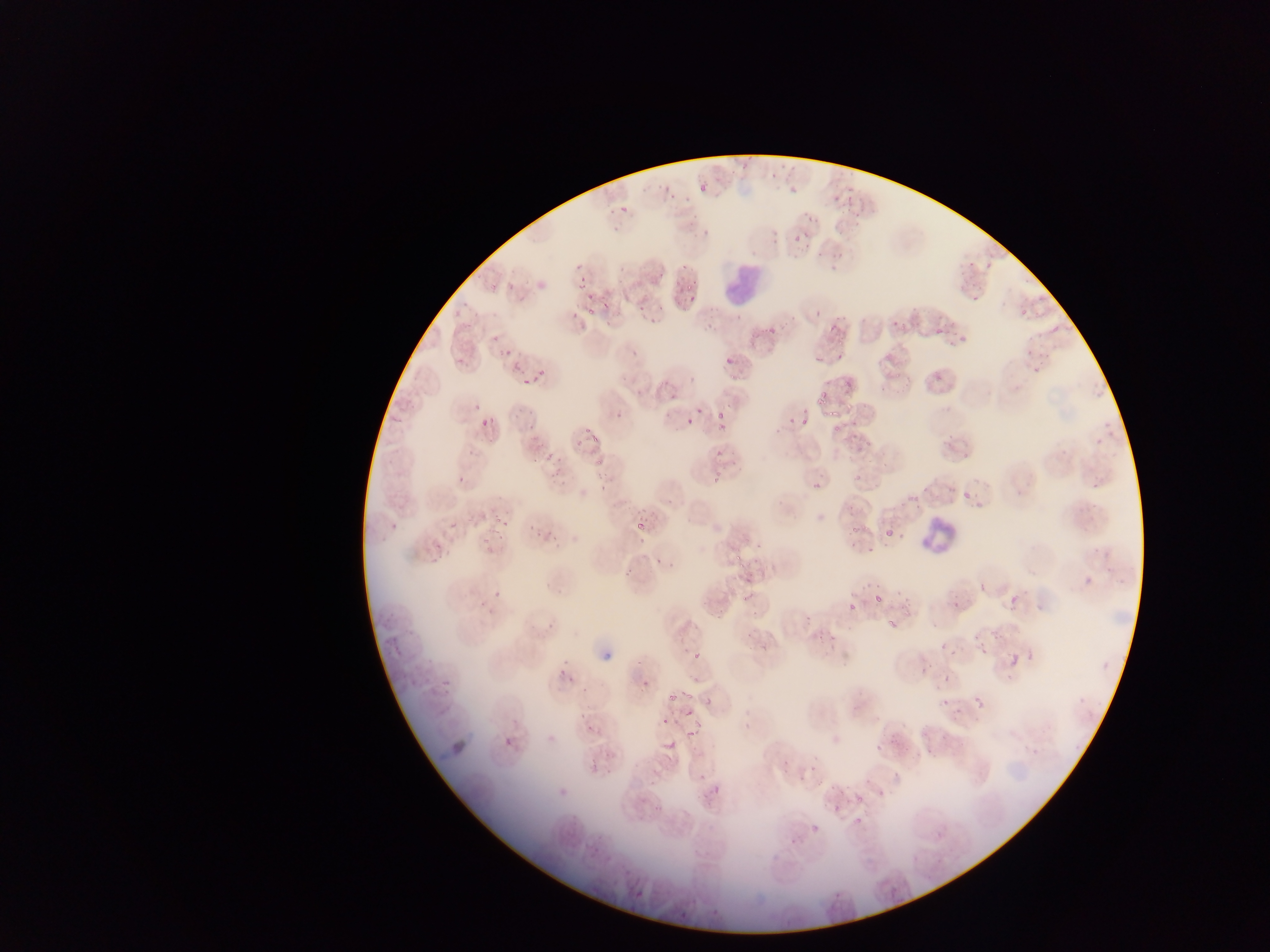

Approximate bounding boxes as [left, top, right, bottom] in pixels. Plasmodium parasite locations: [788, 223, 816, 250], [574, 274, 590, 296], [679, 286, 698, 304], [587, 303, 604, 321], [807, 310, 819, 319], [826, 321, 840, 339], [1050, 324, 1060, 333], [935, 327, 943, 334], [486, 334, 503, 346], [721, 343, 740, 366], [497, 347, 518, 365], [810, 354, 823, 366], [535, 368, 549, 385], [518, 380, 529, 388], [715, 399, 732, 430], [479, 415, 493, 428], [800, 415, 807, 425], [781, 417, 801, 426], [685, 418, 695, 427], [585, 434, 597, 447], [714, 447, 722, 458], [538, 458, 547, 467], [705, 470, 726, 490], [456, 471, 470, 481], [809, 477, 828, 488], [962, 484, 972, 503], [630, 503, 651, 527], [388, 519, 407, 535], [449, 520, 459, 531], [885, 529, 894, 538], [653, 538, 685, 566], [1078, 560, 1097, 586], [487, 583, 511, 597], [980, 585, 987, 594], [875, 595, 884, 604], [883, 601, 904, 631], [849, 604, 856, 612], [804, 615, 813, 624], [688, 646, 706, 662], [979, 647, 987, 656], [1008, 657, 1017, 666], [944, 675, 950, 684], [552, 676, 580, 694], [681, 691, 694, 700], [973, 695, 984, 706], [705, 699, 712, 708], [661, 716, 670, 726], [586, 721, 600, 734], [547, 733, 556, 744], [503, 735, 514, 749], [667, 740, 677, 749], [874, 782, 896, 796], [847, 786, 861, 802], [811, 824, 821, 833], [936, 830, 945, 839], [629, 887, 639, 903] | approximate [x, y] pixel centers of objects too small to bound: [673, 403], [943, 646], [925, 671]. Leukocyte locations: [724, 262, 763, 310], [920, 517, 960, 553]. Image is 1270×952 pixels. Photographed through a microscope with a mobile-phone camera. Single field of view. Thin blood smear. Collected in Ghana.